State which cell type is depicted.
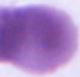
This is an erythrocyte.

1000x magnification. Photomicrograph.